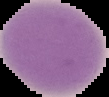
image_type: segmented cell region on a black background
result: negative for Plasmodium parasites
preparation: thin blood smear
image_size: 109×97 pixels